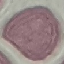

Summary:
  - Malaria status: uninfected
  - Image type: cell patch, automatically extracted from a larger field of view and resized to 64 × 64 pixels
  - Stain: Giemsa
  - Capture: smartphone camera at the microscope eyepiece
  - Preparation: thin blood smear